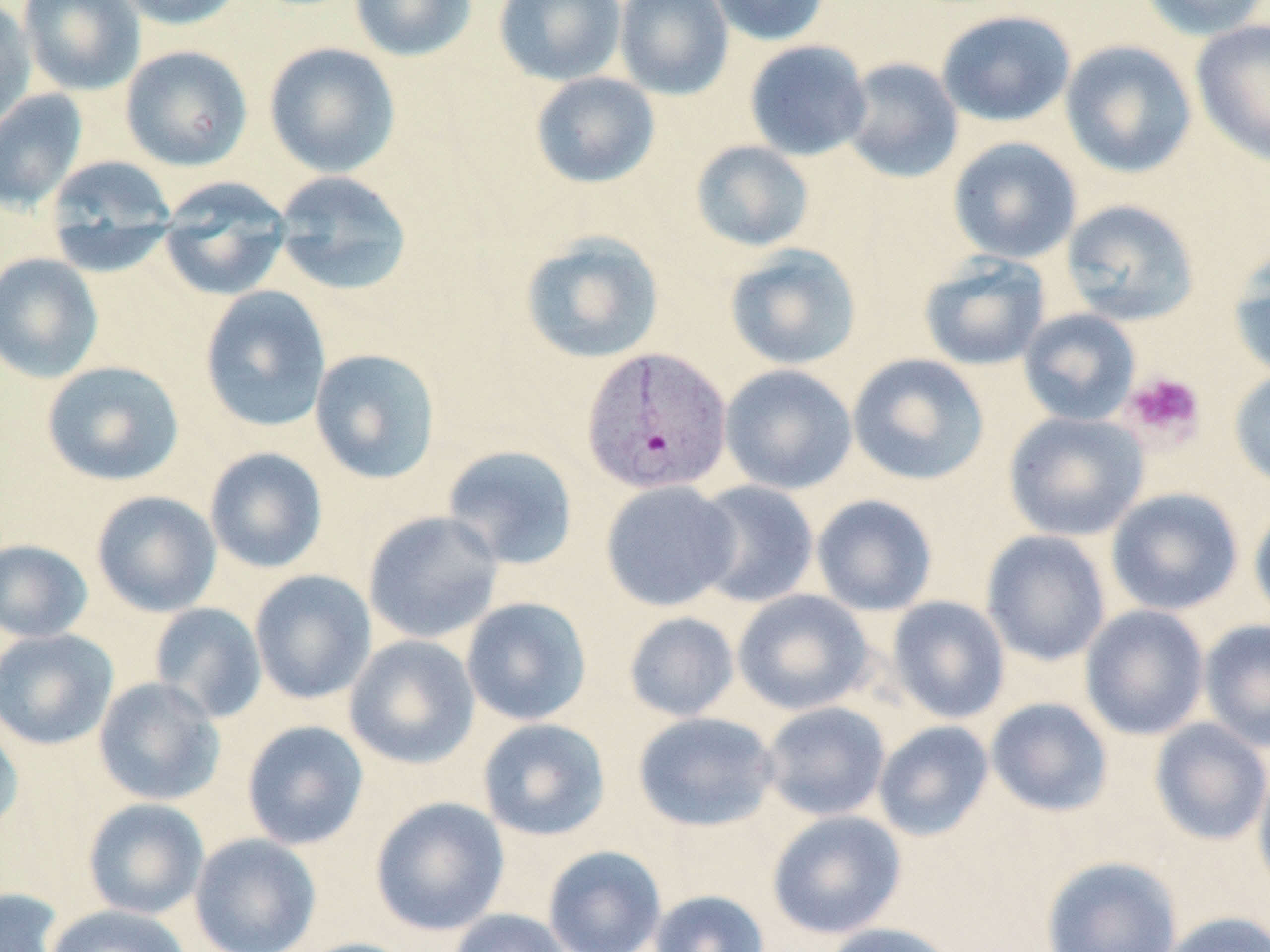

Summary:
  - Coordinate format: approximate bounding boxes as (x1, y1, x2, y2) in pixels
  - Plasmodium vivax-infected red blood cell locations: (581, 346, 733, 496)
  - Platelet locations: (1121, 372, 1205, 445)
  - Uninfected red blood cell locations: (0, 0, 37, 130), (18, 0, 146, 96), (111, 0, 247, 30), (349, 0, 477, 61), (494, 0, 626, 86), (613, 0, 734, 99), (706, 0, 831, 46), (1138, 0, 1269, 41), (936, 10, 1076, 127), (1190, 20, 1270, 167), (1059, 39, 1197, 178), (744, 40, 872, 161), (264, 41, 401, 177), (120, 45, 253, 171), (840, 57, 964, 184), (530, 72, 661, 189), (1, 88, 88, 214), (947, 136, 1082, 264), (690, 140, 815, 252), (43, 155, 178, 273), (272, 170, 414, 296), (157, 179, 293, 300), (1060, 199, 1199, 326), (519, 230, 665, 364), (724, 244, 863, 370), (1228, 247, 1270, 381), (0, 252, 103, 383), (918, 254, 1051, 371), (199, 286, 332, 433), (1018, 308, 1141, 426), (310, 347, 441, 484), (847, 353, 990, 486), (41, 360, 185, 487), (720, 364, 858, 495), (1229, 369, 1270, 490), (1002, 411, 1149, 541), (442, 444, 579, 570), (204, 447, 328, 574), (600, 480, 741, 612), (691, 480, 819, 608), (1106, 487, 1243, 616), (91, 490, 222, 618), (811, 494, 938, 616), (1249, 500, 1270, 627), (363, 510, 505, 644), (980, 530, 1111, 666), (0, 539, 94, 643), (249, 569, 377, 705), (732, 589, 875, 716), (886, 596, 1011, 724), (460, 597, 592, 726), (149, 602, 268, 724), (1080, 604, 1210, 741), (623, 611, 740, 722), (1199, 618, 1270, 753), (0, 628, 119, 750), (344, 634, 480, 769), (93, 676, 226, 806), (985, 697, 1114, 817), (760, 701, 891, 822), (633, 711, 779, 832), (0, 714, 25, 837), (477, 718, 611, 841), (1150, 718, 1270, 846), (241, 720, 369, 850), (873, 720, 995, 841), (1253, 760, 1270, 902), (370, 796, 510, 936), (82, 798, 210, 920), (767, 809, 907, 939), (190, 833, 321, 952), (542, 845, 667, 952), (1040, 856, 1182, 952), (0, 887, 65, 951), (649, 889, 769, 952), (44, 905, 192, 952), (447, 908, 571, 952), (1160, 911, 1270, 952), (820, 922, 960, 952), (292, 937, 421, 952)
  - Slide-level diagnosis: Plasmodium vivax
  - Preparation: thin blood smear
  - Field of view: one of a larger specimen
  - Magnification: 1000x
  - Stain: May-Grünwald-Giemsa
  - Modality: light microscopy
  - Image size: 1270×952 pixels